Identify the parasite.
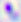
Toxoplasma gondii.

Summary:
  - Magnification: 400x
  - Modality: micrograph